Classify this cell by malaria status.
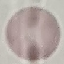
It is uninfected.

{
  "stain": "Giemsa",
  "capture": "smartphone camera at the microscope eyepiece",
  "preparation": "thin blood film",
  "image_type": "automatically extracted cell patch, resized to 64 × 64 pixels"
}